Identify the blood parasite species.
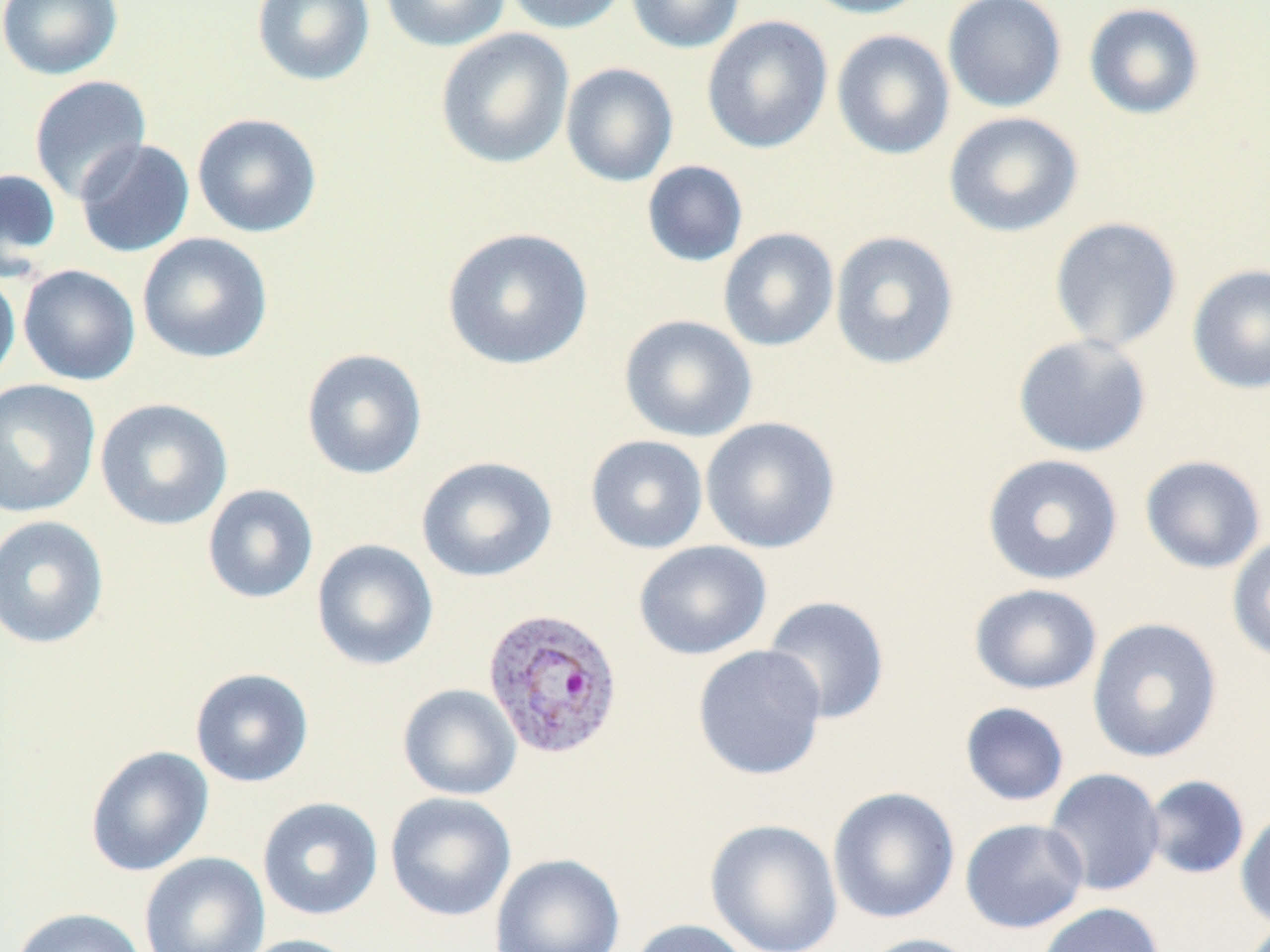

Plasmodium vivax.

Summary:
  - Coordinate format: approximate bounding boxes as [x1, y1, x2, y2] in pixels
  - Uninfected red blood cell locations: [0, 0, 123, 80], [251, 0, 375, 86], [379, 0, 511, 52], [502, 0, 631, 35], [626, 0, 745, 53], [797, 0, 934, 19], [943, 0, 1067, 113], [1083, 2, 1206, 120], [701, 15, 833, 154], [435, 28, 575, 170], [831, 29, 955, 160], [560, 62, 679, 187], [29, 75, 152, 204], [943, 111, 1084, 238], [192, 112, 323, 238], [74, 139, 195, 258], [641, 160, 748, 267], [0, 168, 62, 276], [1048, 216, 1183, 353], [442, 227, 594, 371], [717, 227, 839, 352], [829, 230, 960, 371], [137, 232, 273, 364], [1186, 263, 1270, 394], [17, 264, 140, 386], [0, 267, 21, 389], [619, 314, 758, 442], [1013, 333, 1152, 457], [301, 348, 428, 480], [0, 379, 101, 518], [95, 397, 233, 531], [700, 416, 841, 554], [585, 434, 708, 554], [982, 453, 1123, 585], [416, 455, 557, 583], [1139, 455, 1267, 573], [202, 484, 319, 604], [0, 515, 109, 649], [1226, 534, 1270, 663], [311, 539, 439, 671], [634, 540, 772, 661], [968, 583, 1103, 695], [761, 595, 891, 725], [1087, 617, 1223, 764], [692, 644, 828, 780], [189, 667, 314, 788], [397, 683, 522, 801], [959, 702, 1070, 807], [85, 745, 214, 877], [1043, 768, 1166, 897], [1143, 774, 1251, 880], [827, 786, 960, 924], [384, 791, 516, 922], [257, 797, 383, 921], [1235, 807, 1270, 931], [704, 818, 843, 952], [960, 818, 1089, 934], [138, 851, 270, 952], [489, 853, 625, 952], [1037, 902, 1166, 952], [12, 906, 147, 952], [626, 918, 755, 952], [856, 933, 985, 952], [235, 934, 364, 952]
  - Plasmodium vivax-infected red blood cell locations: [482, 605, 625, 761]
  - Preparation: thin blood smear
  - Modality: optical microscopy
  - Image size: 1270×952 pixels
  - Magnification: 1000x
  - Stain: May-Grünwald-Giemsa
  - Field of view: one of a larger specimen